Report the malaria status of this cell.
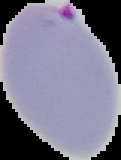

Parasitized.

image_size: 121×160 pixels
image_type: segmented cell region with the area outside set to black
preparation: thin blood smear